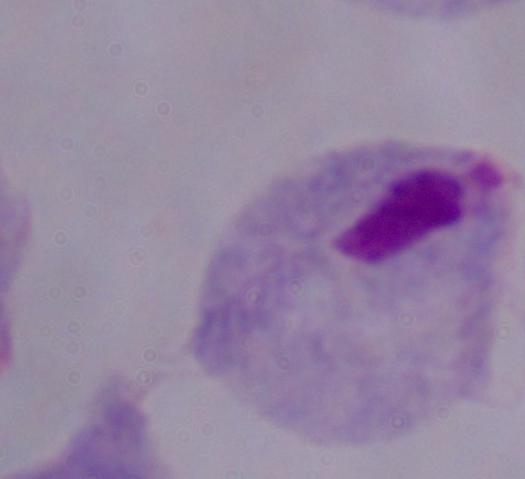
Micrograph. Captured at 1000x magnification. A trichomonad is shown.